Classify this cell by malaria status.
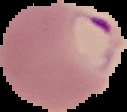
It is parasitized.

image size = 127×112 pixels
preparation = thin blood film
image type = cell region segmented out of the field of view; surrounding area masked to black